Give the position of every malaria parasite.
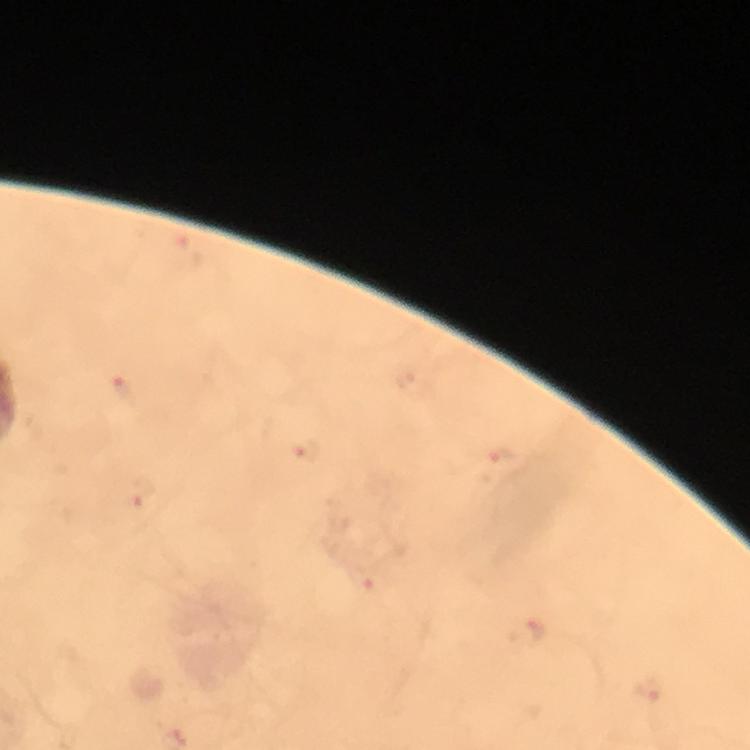
Approximate object centers, in pixels from the top-left corner.
Malaria parasites: (x=121, y=387), (x=306, y=452), (x=501, y=454), (x=142, y=493), (x=366, y=585), (x=538, y=634), (x=649, y=691).

From a diagnostic examination for malaria. Image is 750×750 pixels. Thick smear. Photographed through the microscope with a smartphone camera. Giemsa-stained preparation. Immersion oil applied. A crop from one field of view. At 100x magnification.